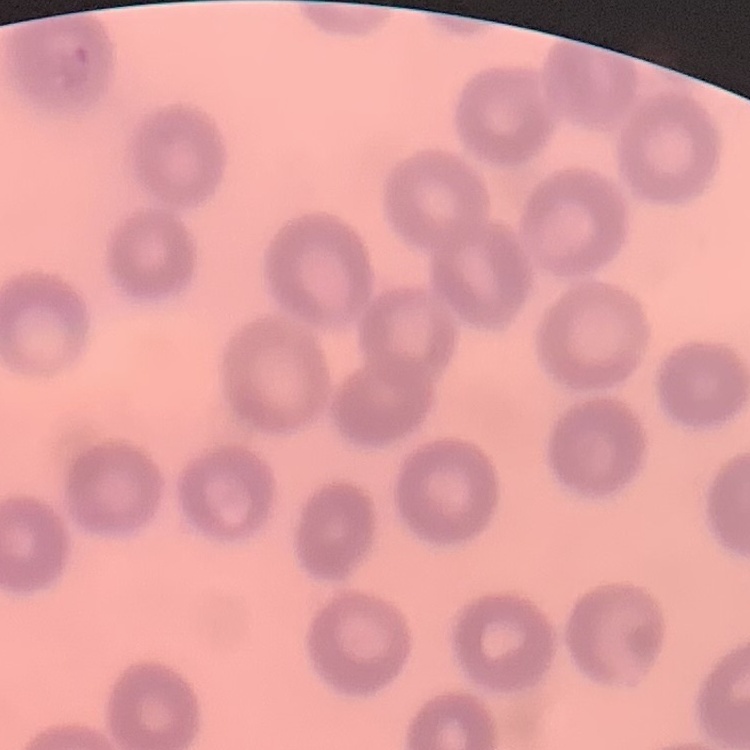

The red blood cells exhibit no rouleaux formation. Field's or Giemsa stain. One tile cut from a larger photomicrograph. Thin peripheral smear.